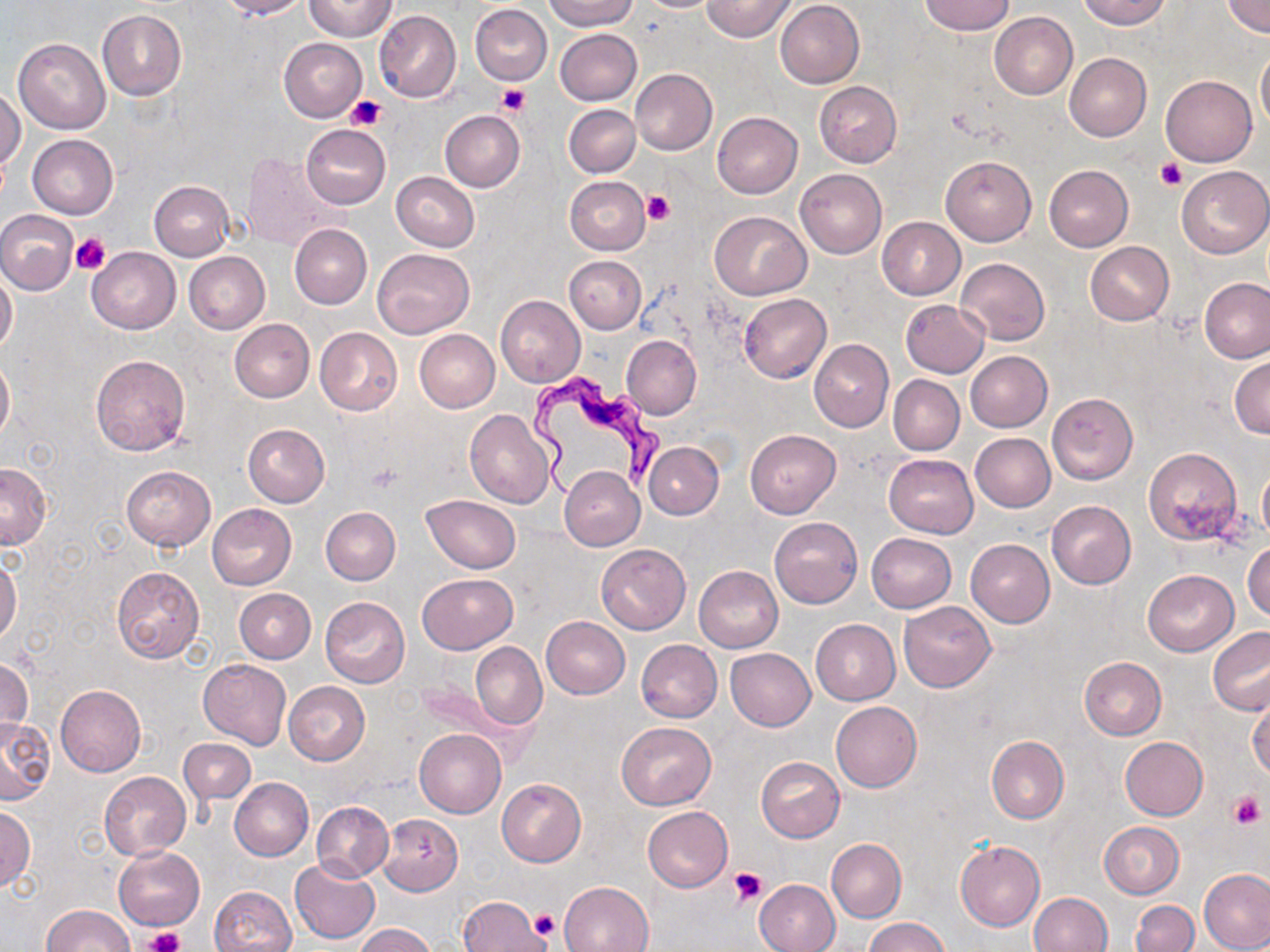
Approximate bounding boxes as (x1, y1, x2, y2) in pixels. Platelet locations: (496, 83, 529, 116), (346, 95, 387, 132), (1156, 160, 1186, 190), (641, 190, 673, 226), (72, 232, 110, 274), (1229, 792, 1264, 829), (730, 866, 767, 906), (532, 908, 559, 940), (144, 927, 185, 952). Uninfected red blood cell locations: (215, 0, 309, 19), (544, 0, 638, 31), (634, 0, 723, 12), (701, 0, 796, 42), (920, 0, 1014, 36), (1078, 0, 1171, 30), (305, 1, 395, 41), (775, 1, 865, 88), (1222, 1, 1270, 37), (470, 4, 552, 85), (97, 10, 188, 100), (374, 10, 461, 102), (989, 12, 1079, 99), (555, 28, 642, 106), (13, 38, 110, 133), (279, 38, 366, 121), (1256, 45, 1270, 132), (1065, 53, 1152, 143), (631, 69, 717, 155), (1162, 76, 1257, 166), (814, 81, 902, 166), (1, 87, 23, 176), (564, 104, 639, 177), (439, 110, 525, 192), (712, 112, 803, 198), (301, 124, 390, 210), (27, 134, 118, 219), (242, 152, 341, 251), (941, 156, 1036, 246), (1044, 164, 1133, 251), (1177, 166, 1270, 259), (795, 168, 887, 258), (392, 171, 479, 252), (565, 176, 650, 255), (149, 180, 235, 261), (0, 211, 78, 294), (710, 212, 810, 300), (877, 217, 966, 300), (289, 223, 372, 309), (1085, 242, 1174, 325), (87, 247, 180, 334), (371, 247, 473, 338), (184, 251, 269, 334), (565, 256, 646, 333), (955, 257, 1050, 345), (0, 269, 17, 356), (1201, 279, 1269, 362), (739, 293, 832, 382), (496, 296, 586, 387), (900, 300, 989, 377), (231, 319, 315, 403), (314, 327, 402, 415), (415, 330, 499, 412), (621, 335, 702, 419), (809, 338, 894, 432), (965, 351, 1052, 432), (0, 354, 13, 442), (90, 355, 190, 456), (1230, 357, 1270, 438), (888, 376, 964, 455), (1046, 393, 1138, 484), (464, 409, 555, 509), (243, 424, 330, 507), (745, 429, 840, 518), (969, 433, 1055, 512), (644, 442, 723, 519), (1144, 448, 1243, 545), (884, 454, 978, 538), (1, 463, 50, 549), (121, 465, 215, 551), (559, 467, 645, 549), (1259, 467, 1270, 542), (422, 495, 521, 573), (1047, 500, 1136, 589), (206, 503, 297, 590), (321, 507, 400, 585), (769, 516, 863, 608), (867, 533, 956, 612), (966, 539, 1054, 627), (1243, 540, 1269, 621), (596, 544, 690, 634), (0, 557, 22, 646), (693, 565, 782, 652), (112, 566, 204, 665), (1143, 569, 1238, 656), (417, 573, 517, 654), (233, 588, 315, 663), (319, 596, 411, 688), (898, 601, 997, 693), (541, 616, 630, 699), (811, 619, 900, 705), (1208, 627, 1270, 716), (636, 639, 722, 723), (471, 642, 547, 729), (725, 648, 815, 731), (0, 656, 32, 743), (1079, 657, 1166, 739), (199, 659, 290, 749), (409, 672, 523, 758), (284, 681, 369, 765), (56, 684, 146, 777), (1247, 693, 1270, 781), (831, 700, 922, 792), (0, 718, 53, 805), (615, 721, 716, 810), (415, 729, 506, 818), (986, 736, 1069, 824), (1120, 736, 1207, 820), (180, 739, 256, 806), (755, 756, 844, 842), (99, 771, 192, 860), (231, 778, 314, 861), (497, 778, 587, 866), (312, 801, 393, 881), (0, 805, 36, 890), (642, 806, 732, 892), (379, 815, 462, 895), (1099, 822, 1184, 899), (827, 838, 906, 922), (955, 840, 1046, 931), (115, 848, 203, 929), (290, 858, 380, 945), (1198, 868, 1270, 952), (210, 872, 375, 947), (754, 878, 840, 952), (558, 881, 654, 952), (209, 885, 297, 952), (1027, 892, 1112, 952), (457, 895, 554, 952), (1131, 900, 1198, 952), (44, 904, 134, 952), (864, 916, 950, 952), (354, 924, 436, 952). Trypanosoma brucei locations: (523, 372, 660, 500). Slide-level diagnosis: Trypanosoma brucei. Light microscopy. Single field of view. Thin blood film. Captured at 1000x magnification. Image is 1270×952 pixels. May-Grünwald-Giemsa-stained preparation.